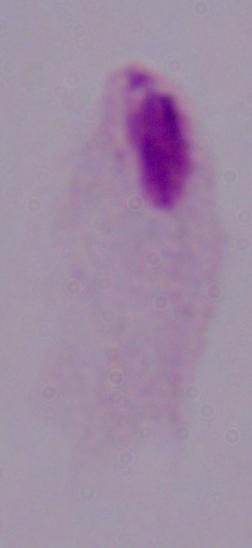
identification = trichomonad
magnification = 1000x
modality = micrograph